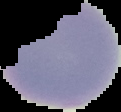

preparation = thin blood smear
image size = 121×112 pixels
result = negative for Plasmodium parasites
image type = segmented cell region on a black background